Identify the parasite.
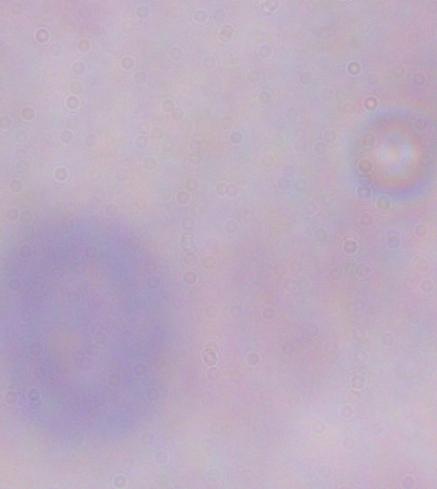

A trypanosome.

Photomicrograph. Captured at 1000x magnification.